Classify the preparation.
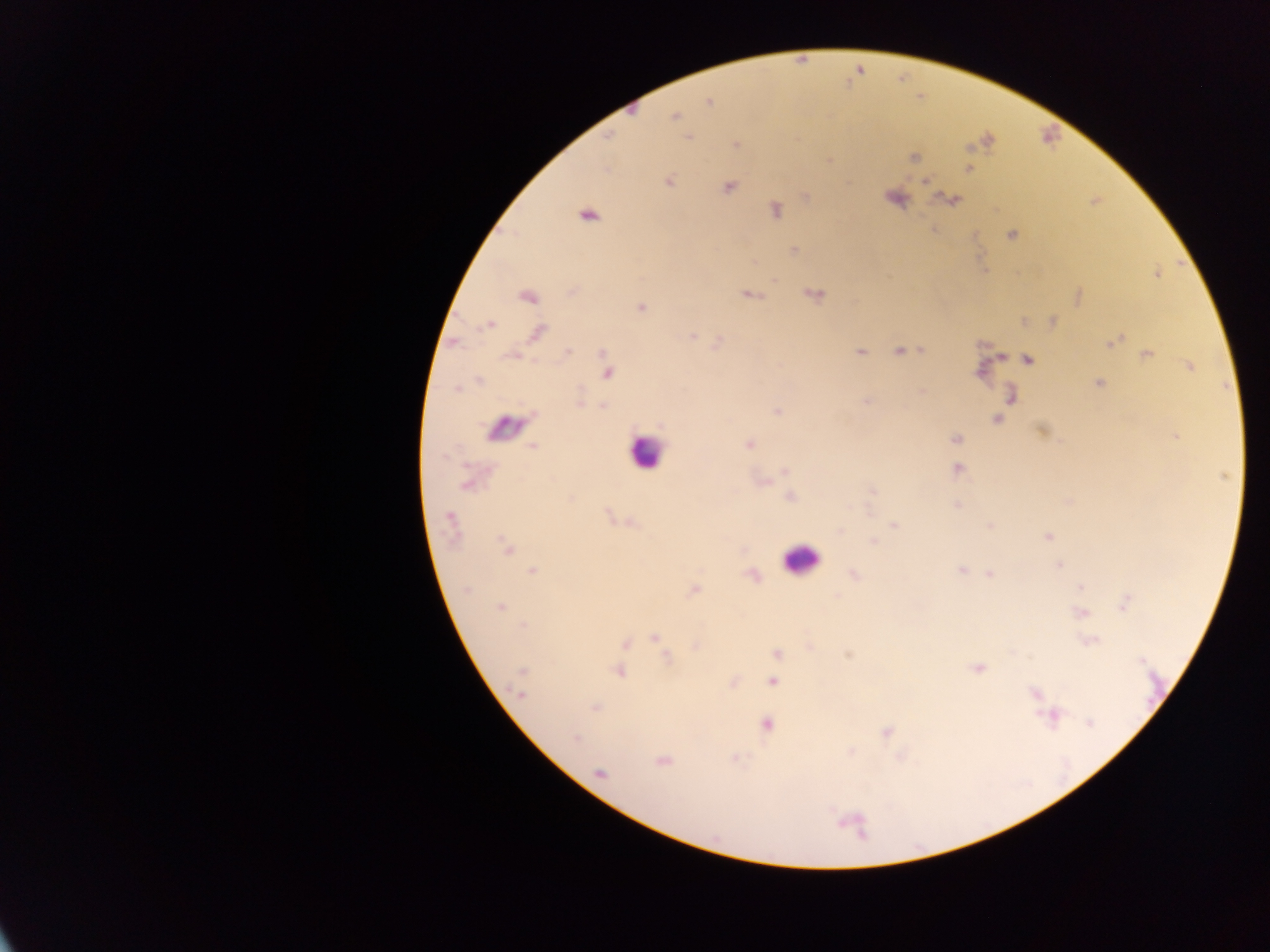
Thick blood smear.

{
  "capture": "mobile-phone photograph through a microscope",
  "country": "Ghana",
  "field_of_view": "single",
  "image_size": "1270×952 pixels",
  "leukocyte_locations": "approximate centers as {x, y} in pixels: {643, 452}, {797, 562}"
}